Describe the morphology of the erythrocytes.
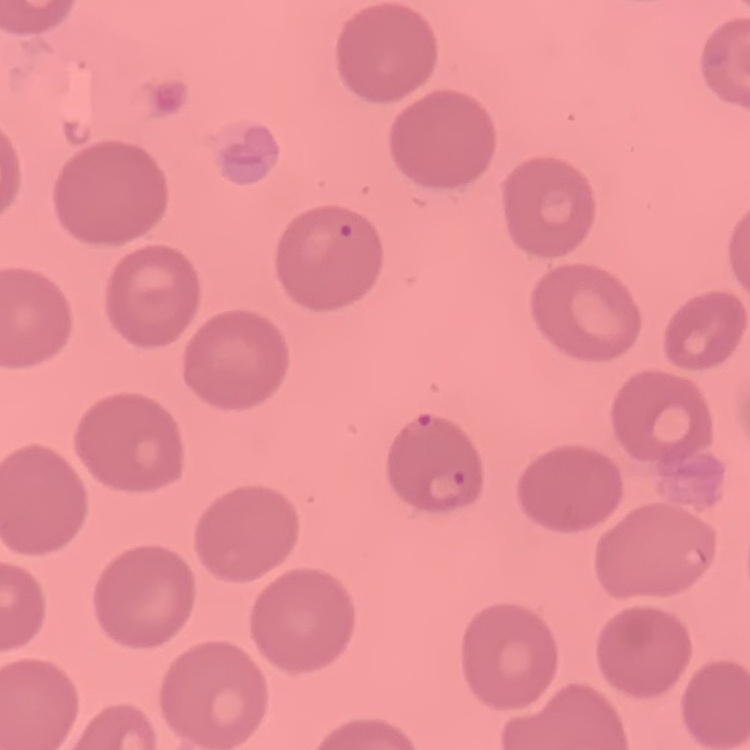
No rouleaux formation.

stain: Field's or Giemsa
preparation: thin blood smear
image_type: one tile cut from a larger photomicrograph